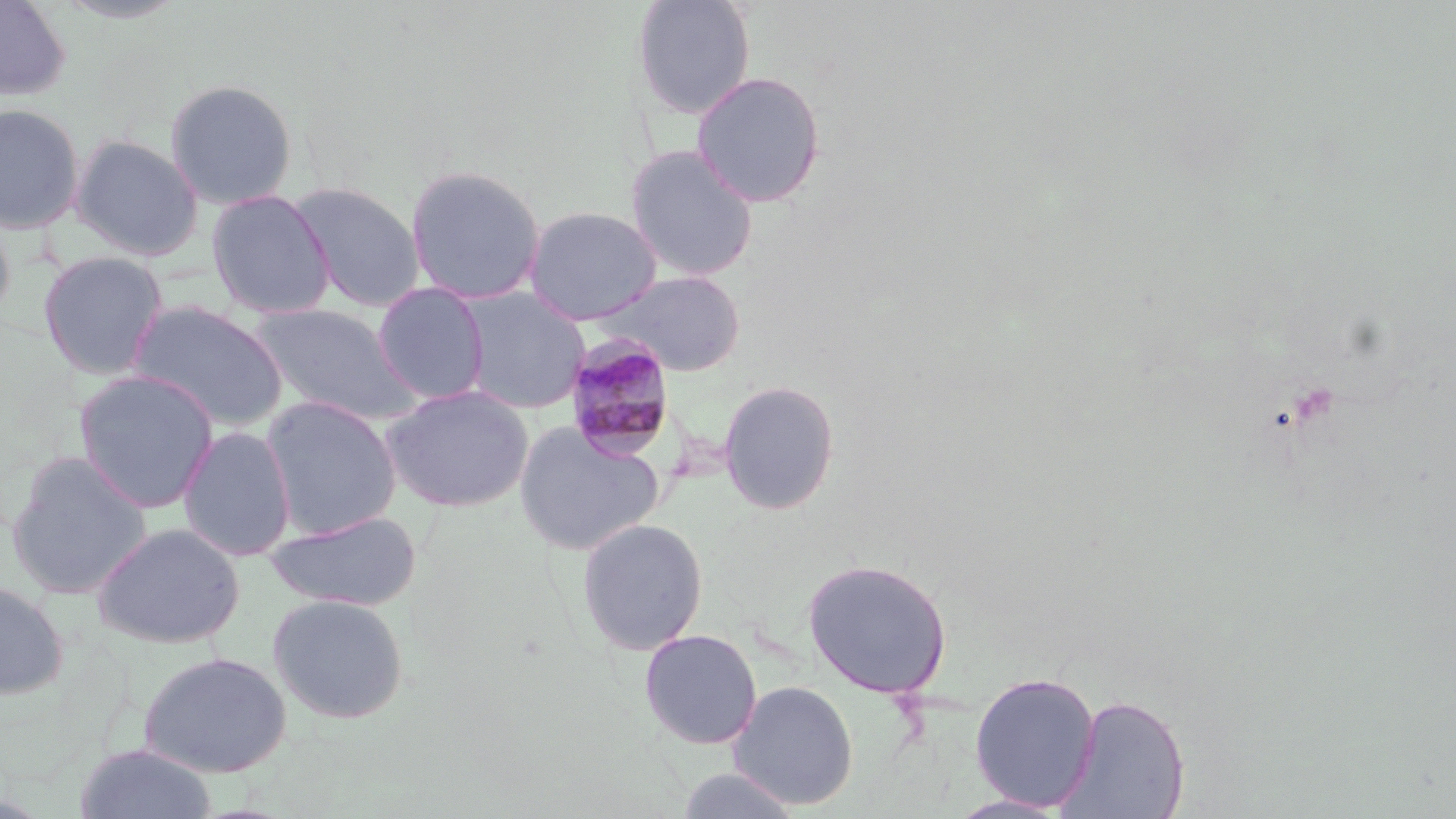

Summary:
  - Coordinate format: approximate bounding boxes as [x1, y1, x2, y2] in pixels
  - Plasmodium malariae-infected red blood cell locations: [562, 336, 679, 463]
  - Uninfected red blood cell locations: [0, 0, 72, 102], [631, 0, 757, 119], [51, 1, 190, 25], [691, 70, 827, 208], [164, 78, 298, 210], [0, 102, 85, 234], [2, 114, 171, 254], [69, 133, 204, 261], [624, 144, 760, 282], [405, 164, 546, 305], [288, 181, 426, 312], [206, 189, 336, 319], [523, 205, 663, 325], [0, 206, 16, 330], [37, 250, 169, 380], [593, 269, 748, 377], [372, 281, 491, 405], [455, 286, 592, 415], [125, 299, 290, 433], [248, 303, 422, 426], [72, 369, 220, 513], [718, 379, 840, 516], [380, 384, 534, 512], [260, 395, 402, 540], [513, 421, 666, 555], [177, 426, 296, 562], [5, 451, 153, 600], [266, 511, 422, 611], [576, 517, 709, 656], [92, 522, 245, 649], [802, 558, 953, 699], [0, 580, 69, 700], [268, 593, 409, 724], [638, 628, 763, 750], [138, 652, 291, 777], [969, 671, 1101, 811], [728, 680, 859, 810], [1058, 694, 1192, 818], [73, 743, 217, 819], [674, 767, 804, 819], [946, 794, 1074, 818]
  - Slide-level diagnosis: Plasmodium malariae
  - Preparation: thin blood film
  - Stain: May-Grünwald-Giemsa
  - Image size: 1456×819 pixels
  - Magnification: 1000x
  - Modality: light microscopy
  - Field of view: single